Evaluate for Plasmodium parasites.
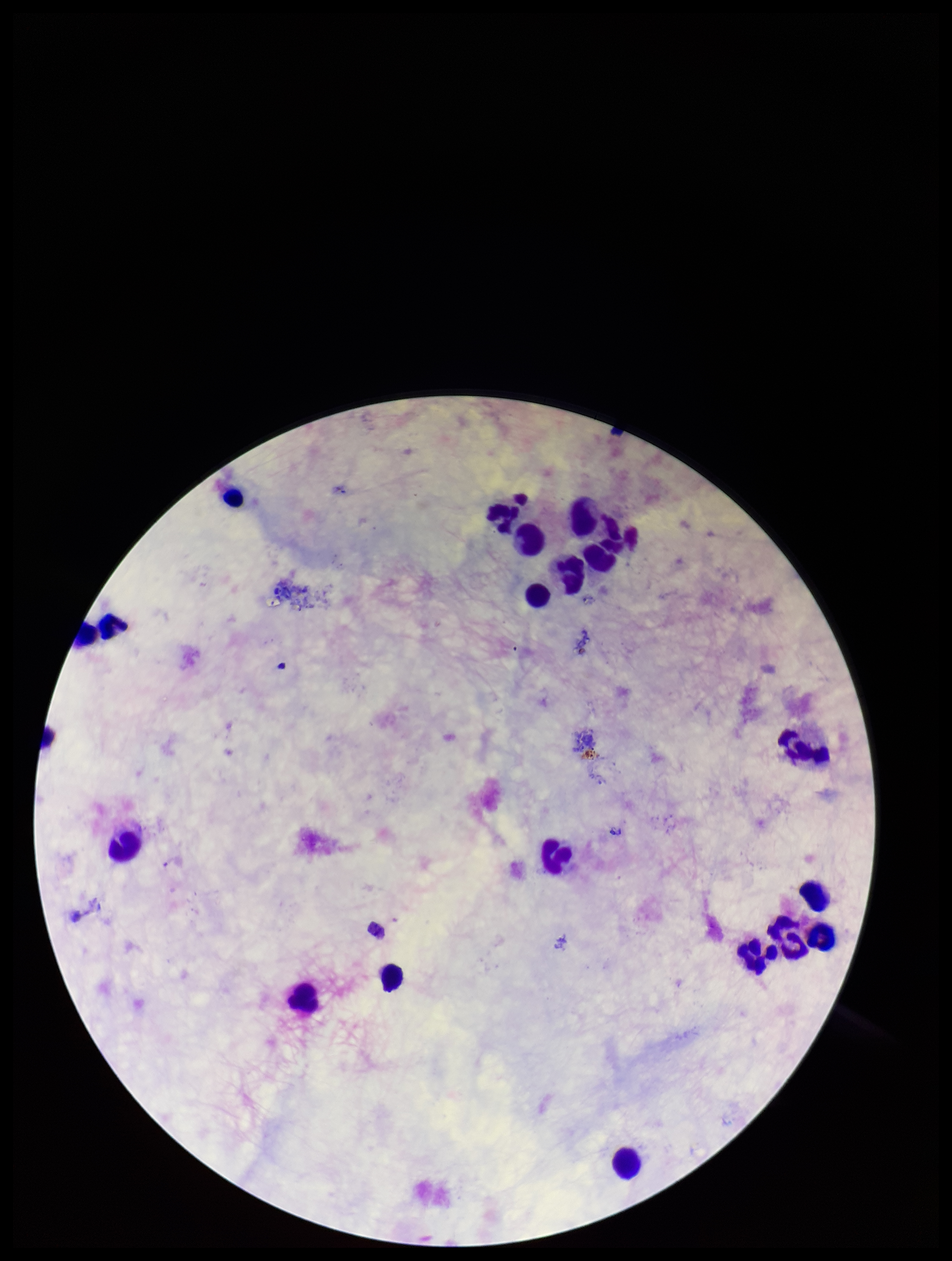

None seen.

preparation = thick blood smear
field of view = single
image size = 952×1261 pixels
leukocyte count = 17
parasite count = 0
stain = Giemsa
capture = smartphone photograph through the microscope eyepiece
patient malaria status = negative